Locate every leukocyte (white blood cell).
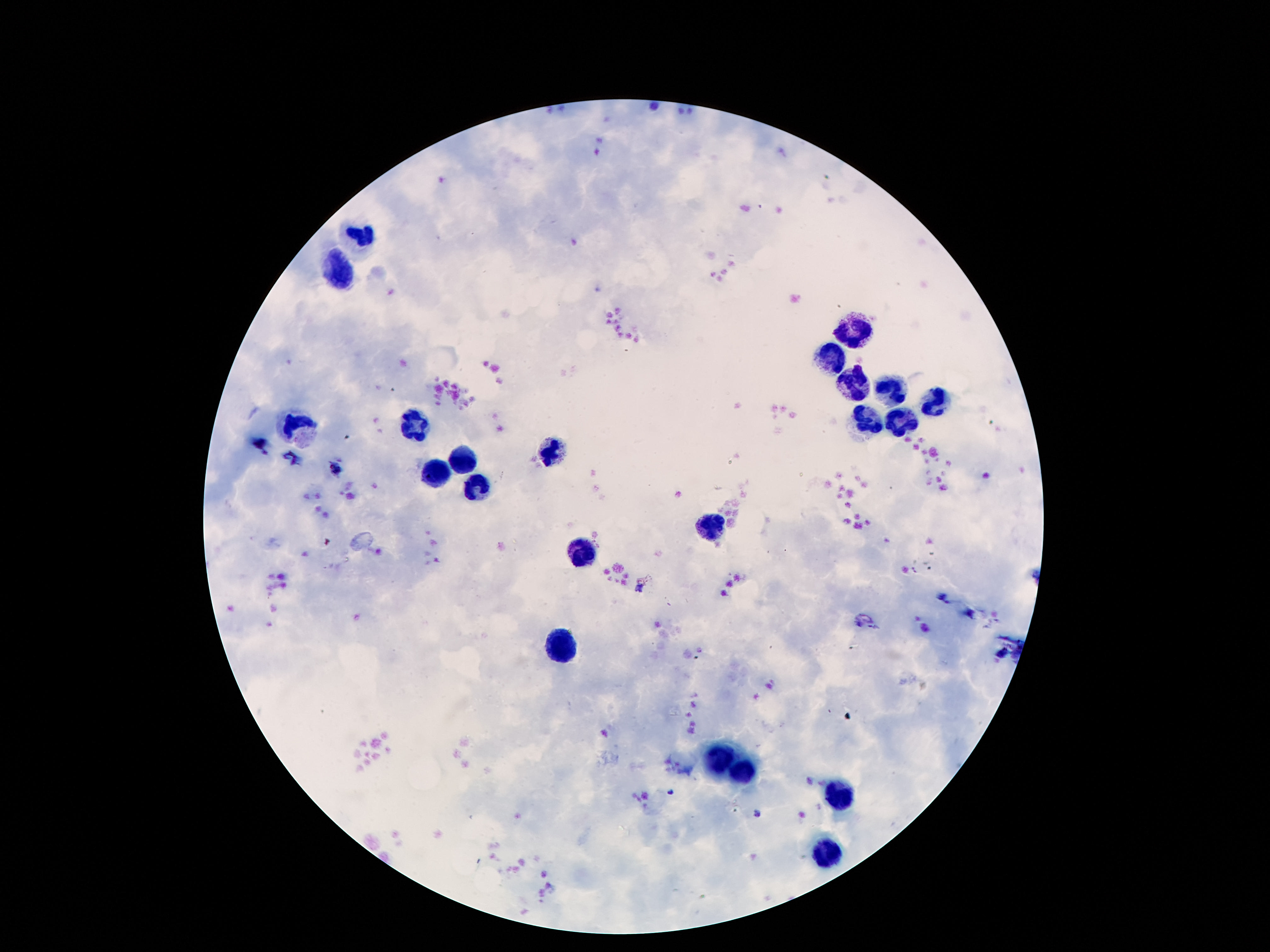

Approximate centers as [x, y] in pixels.
Leukocytes: [364, 233], [339, 273], [864, 330], [837, 357], [855, 385], [889, 390], [931, 399], [870, 420], [301, 424], [417, 424], [897, 424], [549, 453], [461, 460], [438, 472], [477, 487], [715, 527], [585, 556], [561, 647], [715, 757], [744, 774], [843, 793], [830, 857].

Summary:
  - Image size: 1270×952 pixels
  - Patient malaria status: uninfected
  - Stain: Giemsa
  - Field of view: single
  - Preparation: thick blood smear
  - Magnification: 100x
  - Capture: smartphone camera through the microscope eyepiece